Locate every blood parasite and identify its species.
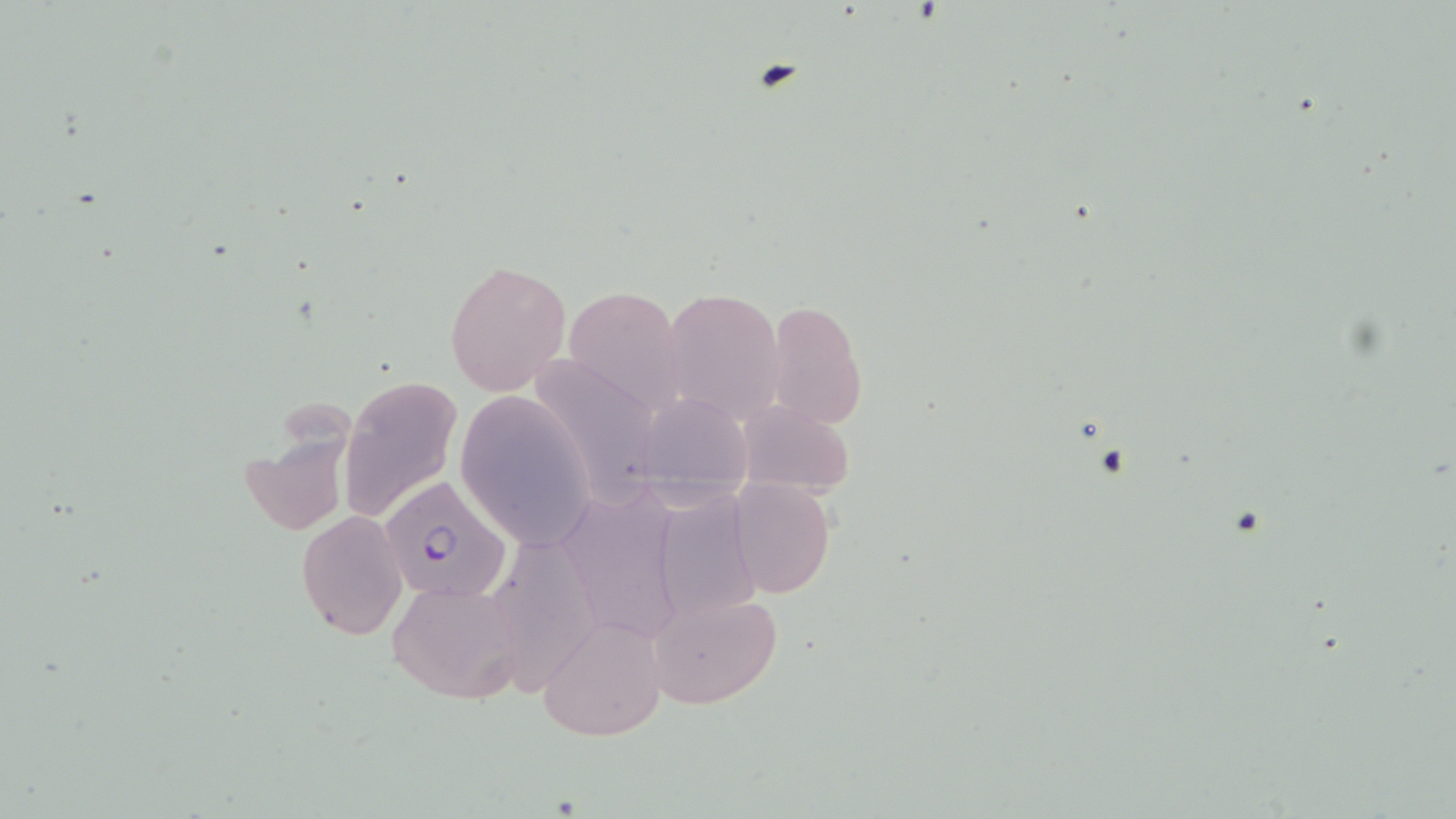
Approximate bounding boxes as named x1/y1/x2/y2 corners in pixels.
Plasmodium falciparum-infected red blood cells: (x1=380, y1=477, x2=511, y2=602).
No Plasmodium ovale, Plasmodium malariae, Plasmodium vivax, Babesia divergens, or Trypanosoma brucei observed.

slide-level diagnosis = Plasmodium falciparum
magnification = 1000x
field of view = single
preparation = thin blood smear
uninfected red blood cell locations = approximate bounding boxes as named x1/y1/x2/y2 corners in pixels: (x1=444, y1=258, x2=571, y2=398), (x1=561, y1=283, x2=689, y2=420), (x1=657, y1=286, x2=785, y2=427), (x1=763, y1=298, x2=868, y2=429), (x1=525, y1=353, x2=663, y2=499), (x1=339, y1=376, x2=463, y2=522), (x1=634, y1=390, x2=753, y2=490), (x1=455, y1=392, x2=595, y2=550), (x1=232, y1=393, x2=371, y2=548), (x1=732, y1=394, x2=856, y2=498), (x1=727, y1=478, x2=836, y2=600), (x1=571, y1=485, x2=685, y2=639), (x1=672, y1=493, x2=763, y2=638), (x1=296, y1=510, x2=408, y2=641), (x1=503, y1=544, x2=602, y2=700), (x1=387, y1=578, x2=529, y2=704), (x1=647, y1=590, x2=782, y2=709), (x1=536, y1=615, x2=668, y2=742)
image size = 1456×819 pixels
stain = May-Grünwald-Giemsa
modality = light microscopy